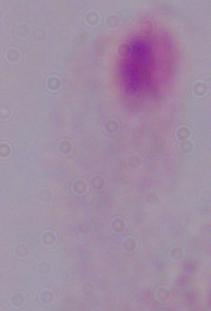

identification: trichomonad
modality: micrograph
magnification: 1000x